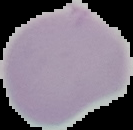
Summary:
  - Image type: segmented cell region with the area outside set to black
  - Preparation: thin blood smear
  - Image size: 133×130 pixels
  - Malaria status: uninfected